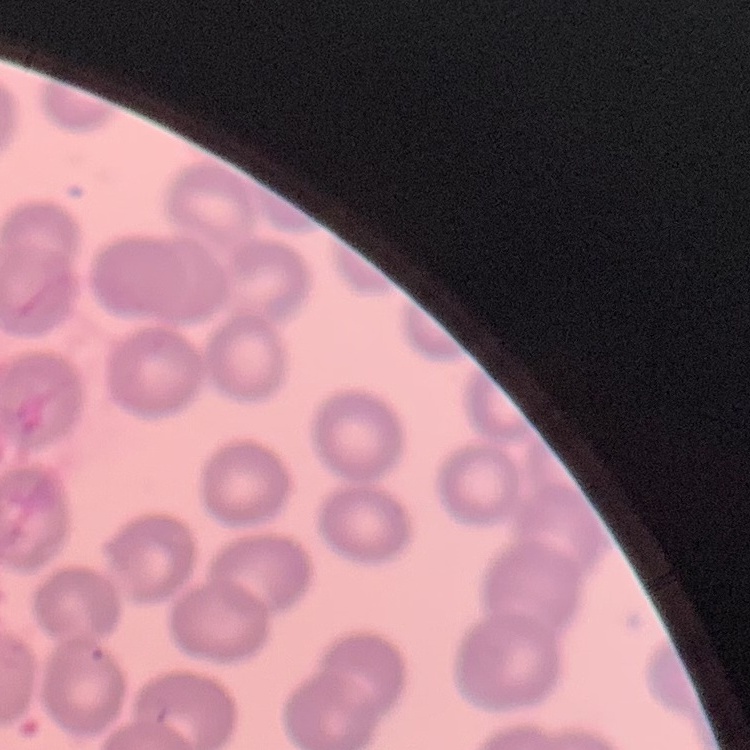 The red blood cells show no rouleaux formation. One tile cut from a larger photomicrograph. Field's or Giemsa stain. Thin blood film.